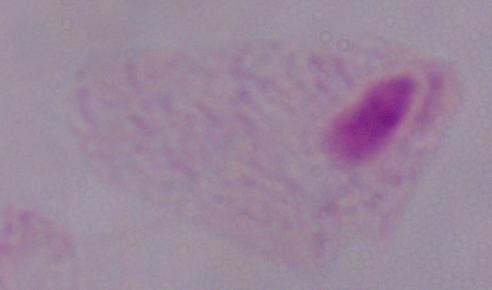

Summary:
  - Identification: trichomonad
  - Modality: photomicrograph
  - Magnification: 1000x